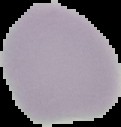

Image is 121×127 pixels. From a thin blood smear. Cell region segmented out of the field of view; the surrounding area is masked to black. Result: no malaria parasites detected.